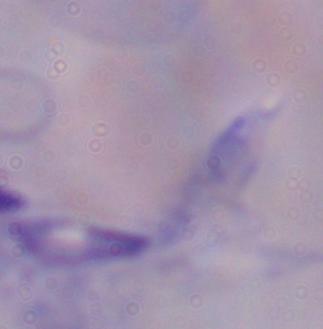

Photomicrograph. A trypanosome is shown. Captured at 1000x magnification.